Locate every Trypanosoma brucei.
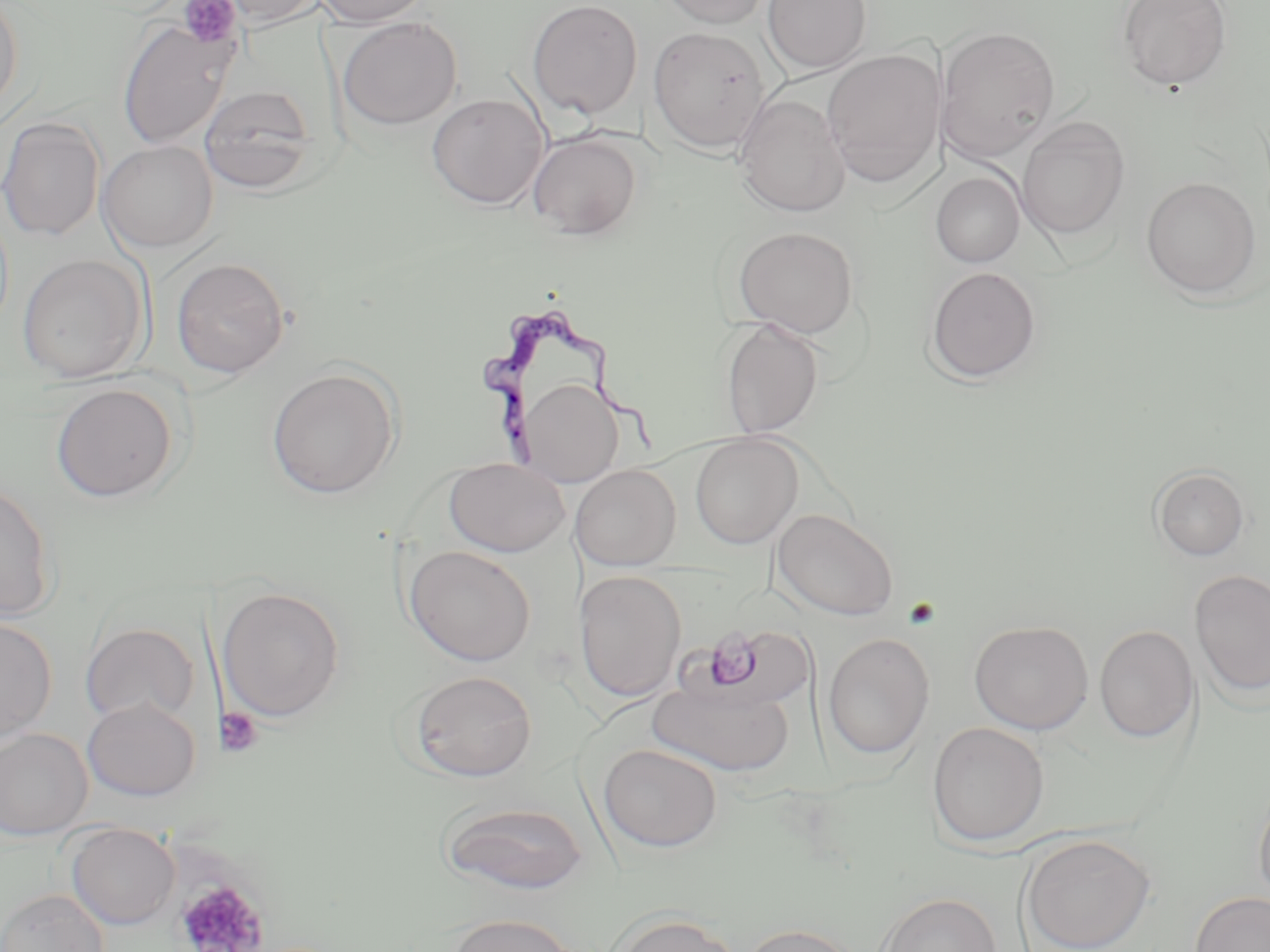

Approximate bounding boxes as named x1/y1/x2/y2 corners in pixels.
Trypanosoma brucei: (x1=481, y1=310, x2=664, y2=462).

Summary:
  - Platelet locations: (x1=178, y1=0, x2=241, y2=48), (x1=703, y1=629, x2=762, y2=689), (x1=216, y1=706, x2=263, y2=758), (x1=176, y1=877, x2=267, y2=952)
  - Uninfected red blood cell locations: (x1=216, y1=0, x2=324, y2=26), (x1=313, y1=0, x2=433, y2=26), (x1=527, y1=0, x2=643, y2=119), (x1=655, y1=0, x2=776, y2=29), (x1=762, y1=0, x2=871, y2=74), (x1=1117, y1=0, x2=1232, y2=91), (x1=0, y1=1, x2=24, y2=115), (x1=337, y1=16, x2=463, y2=130), (x1=117, y1=18, x2=239, y2=150), (x1=936, y1=25, x2=1060, y2=159), (x1=648, y1=26, x2=770, y2=153), (x1=822, y1=49, x2=944, y2=188), (x1=199, y1=84, x2=317, y2=193), (x1=427, y1=92, x2=549, y2=209), (x1=734, y1=93, x2=851, y2=217), (x1=0, y1=115, x2=105, y2=242), (x1=1017, y1=117, x2=1130, y2=240), (x1=527, y1=131, x2=644, y2=239), (x1=97, y1=140, x2=218, y2=253), (x1=931, y1=171, x2=1025, y2=267), (x1=1141, y1=176, x2=1262, y2=298), (x1=733, y1=226, x2=860, y2=338), (x1=16, y1=252, x2=150, y2=383), (x1=171, y1=257, x2=289, y2=378), (x1=925, y1=266, x2=1042, y2=383), (x1=720, y1=318, x2=825, y2=439), (x1=266, y1=367, x2=401, y2=499), (x1=517, y1=377, x2=623, y2=486), (x1=49, y1=382, x2=179, y2=502), (x1=690, y1=433, x2=803, y2=549), (x1=444, y1=457, x2=569, y2=557), (x1=571, y1=464, x2=681, y2=570), (x1=1150, y1=466, x2=1250, y2=561), (x1=0, y1=481, x2=57, y2=622), (x1=773, y1=508, x2=898, y2=621), (x1=404, y1=545, x2=536, y2=667), (x1=1190, y1=569, x2=1270, y2=699), (x1=573, y1=570, x2=686, y2=702), (x1=216, y1=586, x2=346, y2=723), (x1=0, y1=615, x2=58, y2=744), (x1=969, y1=620, x2=1094, y2=734), (x1=80, y1=622, x2=200, y2=725), (x1=1094, y1=624, x2=1198, y2=743), (x1=698, y1=625, x2=814, y2=709), (x1=822, y1=632, x2=935, y2=760), (x1=409, y1=670, x2=537, y2=782), (x1=648, y1=676, x2=795, y2=777), (x1=82, y1=698, x2=201, y2=801), (x1=927, y1=722, x2=1049, y2=846), (x1=0, y1=728, x2=93, y2=841), (x1=598, y1=743, x2=722, y2=852), (x1=1254, y1=784, x2=1270, y2=911), (x1=438, y1=801, x2=591, y2=894), (x1=65, y1=822, x2=181, y2=930), (x1=1019, y1=833, x2=1156, y2=952), (x1=0, y1=888, x2=110, y2=952), (x1=1189, y1=891, x2=1270, y2=952), (x1=875, y1=892, x2=1001, y2=952), (x1=608, y1=912, x2=744, y2=952), (x1=444, y1=913, x2=579, y2=952), (x1=739, y1=922, x2=861, y2=952)
  - Slide-level diagnosis: Trypanosoma brucei
  - Preparation: thin blood smear
  - Stain: May-Grünwald-Giemsa
  - Modality: light microscopy
  - Image size: 1270×952 pixels
  - Field of view: one of a larger specimen
  - Magnification: 1000x